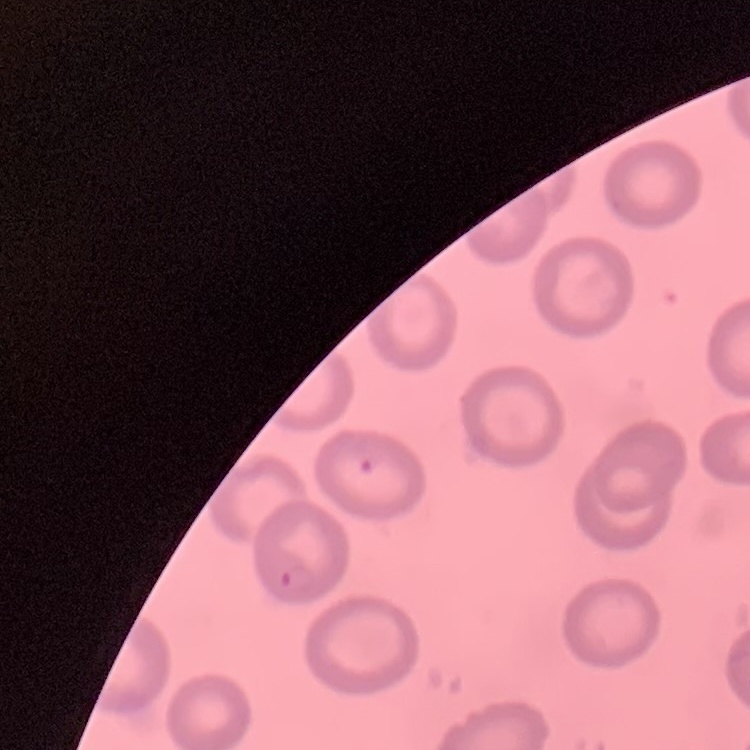
The red blood cells show no rouleaux formation. Stained with either Field's or Giemsa. Square crop of a larger photomicrograph. Thin blood smear.